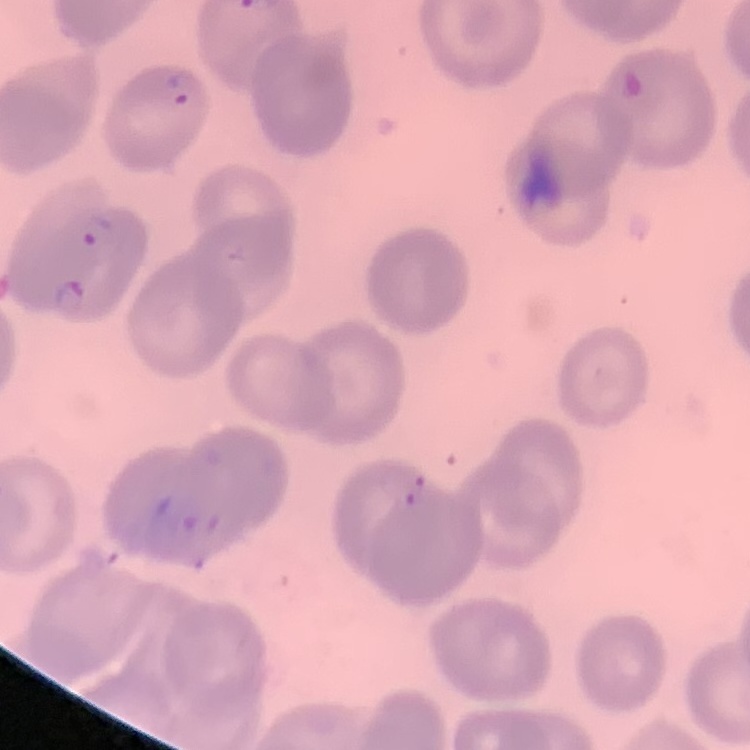
The red blood cells show no rouleaux formation. Stained with either Field's or Giemsa. One tile cut from a larger photomicrograph. Thin peripheral smear.